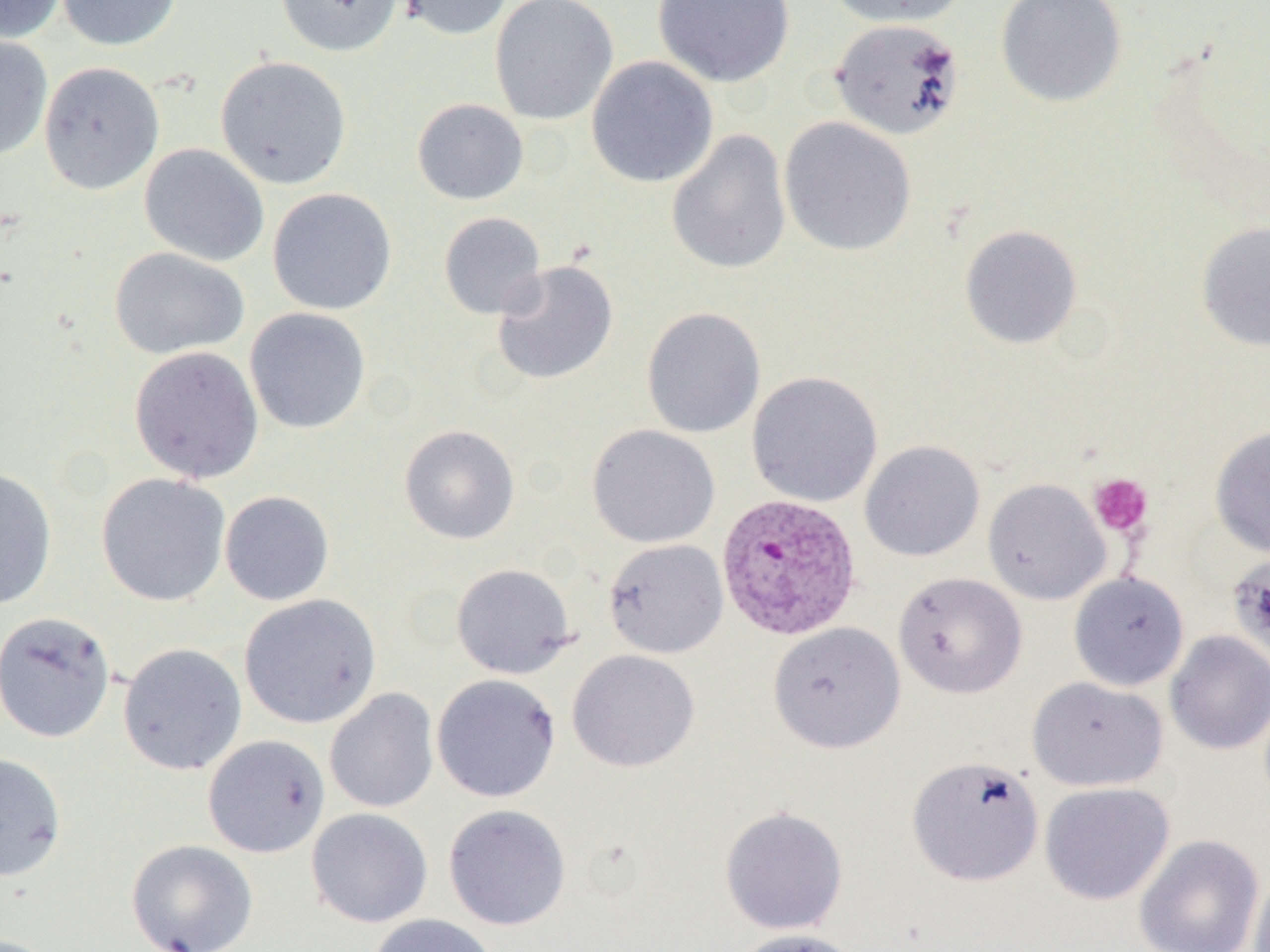
Approximate bounding boxes as (x1, y1, x2, y2) in pixels. Uninfected red blood cell locations: (1, 0, 67, 44), (56, 0, 182, 51), (274, 0, 404, 57), (394, 0, 516, 40), (489, 0, 619, 126), (652, 0, 795, 87), (827, 0, 967, 28), (995, 0, 1128, 108), (829, 17, 966, 140), (0, 34, 53, 161), (215, 55, 352, 189), (586, 56, 718, 188), (38, 61, 165, 195), (411, 98, 529, 205), (779, 116, 917, 256), (666, 129, 792, 275), (139, 143, 270, 267), (267, 187, 397, 315), (438, 212, 546, 320), (1196, 221, 1270, 352), (959, 224, 1083, 349), (109, 247, 249, 361), (491, 259, 619, 386), (244, 307, 371, 433), (641, 307, 766, 439), (129, 346, 264, 484), (746, 371, 883, 508), (398, 424, 520, 545), (586, 424, 720, 548), (1209, 426, 1270, 557), (860, 440, 985, 562), (0, 467, 57, 610), (96, 472, 231, 607), (983, 479, 1111, 605), (220, 490, 334, 606), (602, 538, 729, 659), (1228, 551, 1270, 660), (451, 562, 576, 679), (1068, 571, 1190, 691), (893, 572, 1027, 699), (239, 593, 381, 729), (0, 610, 116, 743), (767, 621, 906, 753), (1164, 631, 1270, 755), (118, 642, 247, 775), (567, 649, 700, 773), (431, 673, 562, 803), (1027, 676, 1169, 792), (325, 688, 439, 813), (202, 734, 330, 858), (0, 752, 66, 882), (906, 755, 1045, 887), (1039, 781, 1175, 905), (443, 804, 572, 930), (719, 806, 848, 935), (306, 807, 433, 928), (1133, 834, 1265, 952), (127, 839, 258, 952), (1249, 866, 1270, 952), (366, 913, 500, 952), (729, 928, 867, 952). Plasmodium vivax-infected red blood cell locations: (716, 493, 862, 641). Platelet locations: (1088, 473, 1153, 537). Slide-level diagnosis: Plasmodium vivax. Captured at 1000x magnification. Optical microscopy. Image is 1270×952 pixels. Single field of view. Thin blood smear.